Report the malaria status of this cell.
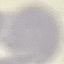

Uninfected.

Thin blood smear. Automatically extracted cell patch, resized to 64 × 64 pixels. Giemsa-stained preparation. Acquired by smartphone through the microscope eyepiece.